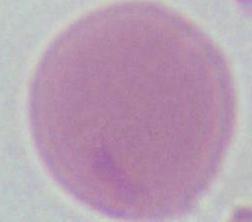

{
  "identification": "red blood cell",
  "magnification": "1000x",
  "modality": "photomicrograph"
}